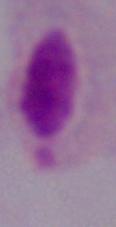

Captured at 1000x magnification. A trichomonad is shown. Photomicrograph.